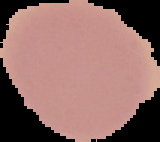

preparation = thin blood smear
image type = segmented cell region on a black background
image size = 160×142 pixels
malaria status = uninfected